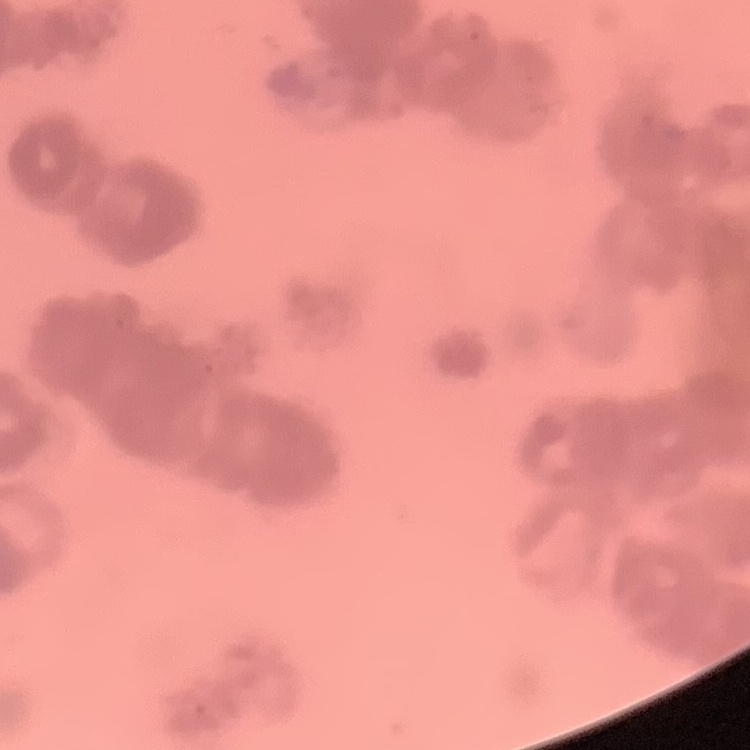

The erythrocytes show rouleaux formation. Square crop of a larger photomicrograph. Thin blood film. Stained with either Field's or Giemsa.